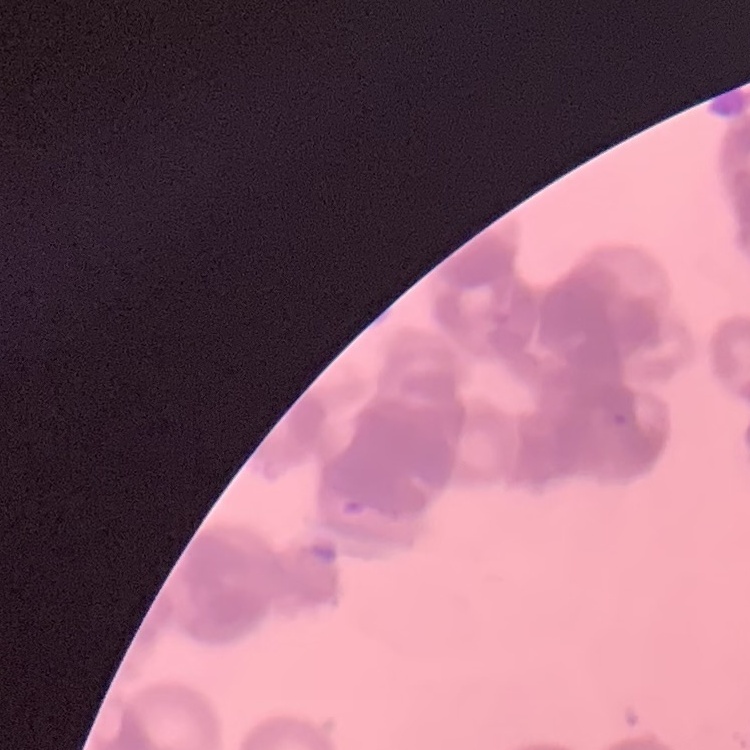
Summary:
  - Erythrocyte morphology: rouleaux formation
  - Stain: Field's or Giemsa
  - Image type: square crop of a larger photomicrograph
  - Preparation: thin peripheral smear